Assess this cell for malaria.
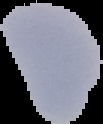

It is uninfected.

Summary:
  - Preparation: thin blood film
  - Image size: 103×124 pixels
  - Image type: cell region segmented out of the field of view; surrounding area masked to black